Locate every uninfected red blood cell.
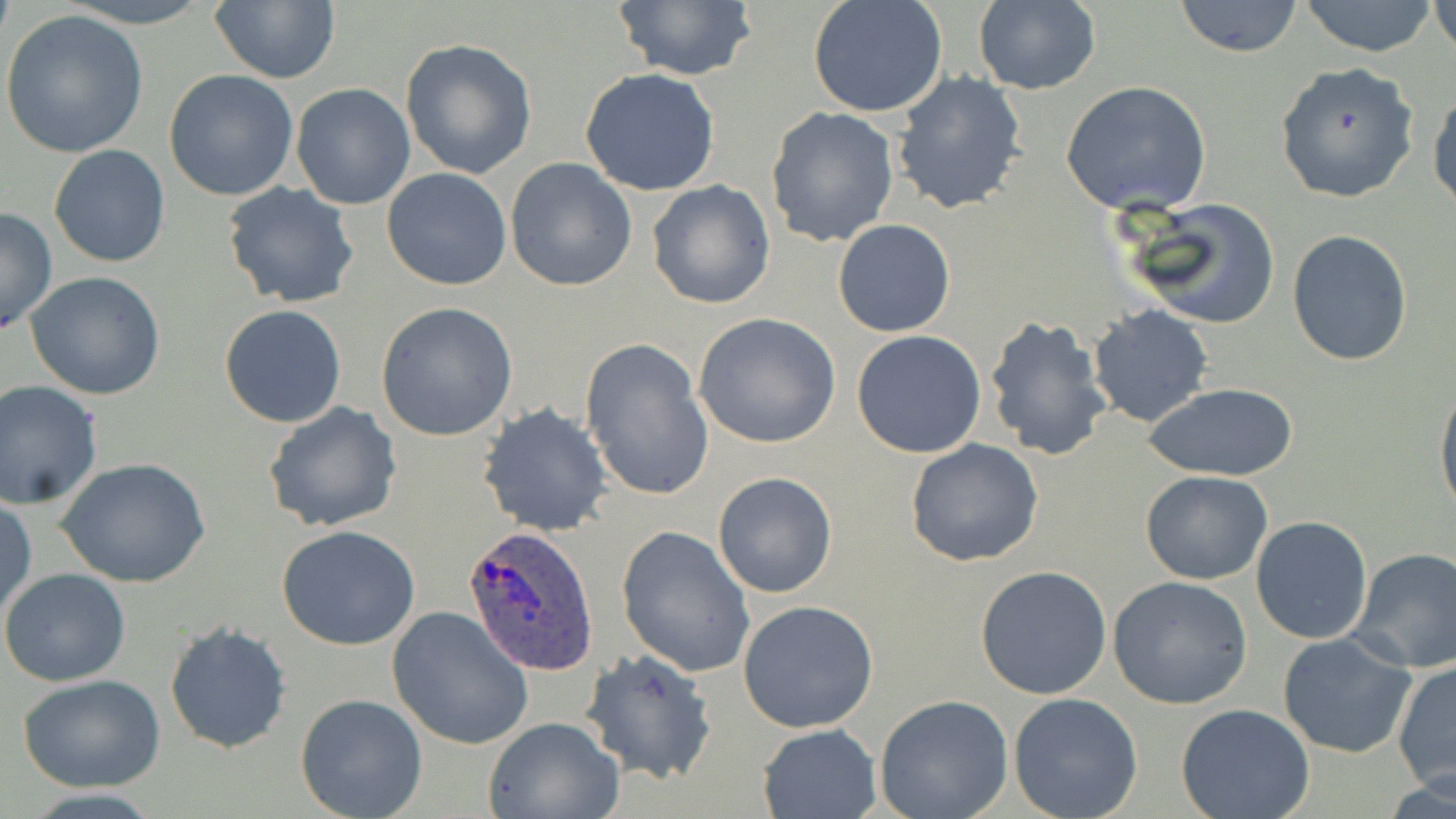
Approximate bounding boxes as (x1,y1)-(x2,y2) corner pairs in pixels.
Uninfected red blood cells: (64,0)-(215,27), (608,0)-(758,83), (808,0)-(948,119), (1297,0)-(1441,57), (208,1)-(341,84), (1172,1)-(1305,57), (1431,1)-(1456,60), (972,2)-(1100,94), (1,10)-(150,159), (400,38)-(537,180), (1274,61)-(1421,204), (579,68)-(721,197), (164,70)-(298,201), (891,71)-(1027,215), (1061,80)-(1213,216), (291,83)-(415,209), (1429,88)-(1455,215), (765,107)-(899,248), (49,144)-(170,268), (505,157)-(638,292), (381,167)-(512,292), (647,180)-(776,310), (222,183)-(360,308), (1121,197)-(1281,330), (0,207)-(56,336), (832,218)-(955,338), (1286,229)-(1413,367), (24,271)-(166,400), (375,302)-(517,441), (219,303)-(347,428), (1088,305)-(1214,428), (693,312)-(842,449), (982,314)-(1113,462), (851,330)-(986,459), (578,335)-(714,504), (0,382)-(104,509), (1435,382)-(1456,522), (1146,383)-(1296,481), (262,402)-(403,536), (478,403)-(614,538), (904,440)-(1044,568), (58,457)-(211,590), (1131,469)-(1264,703), (712,471)-(837,597), (1140,471)-(1274,584), (0,496)-(36,624), (1250,516)-(1375,645), (276,525)-(421,650), (616,525)-(755,677), (1348,547)-(1456,674), (975,565)-(1112,699), (0,567)-(131,686), (1108,576)-(1252,708), (737,600)-(880,734), (387,606)-(533,751), (164,622)-(293,754), (1276,632)-(1420,759), (579,648)-(717,784), (1393,660)-(1456,793), (15,674)-(167,792), (1008,692)-(1144,819), (294,693)-(427,819), (873,694)-(1014,819), (1176,702)-(1316,819), (482,716)-(625,819), (756,723)-(882,818).

Summary:
  - Plasmodium ovale-infected red blood cell locations: (460,524)-(599,678)
  - Slide-level diagnosis: Plasmodium ovale
  - Stain: May-Grünwald-Giemsa
  - Field of view: one of a larger specimen
  - Magnification: 1000x
  - Image size: 1456×819 pixels
  - Modality: optical microscopy
  - Preparation: thin blood film